Assess this cell for malaria.
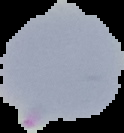
It is parasitized.

{
  "preparation": "thin blood smear",
  "image_size": "124×133 pixels",
  "image_type": "cell region segmented out of the field of view; surrounding area masked to black"
}